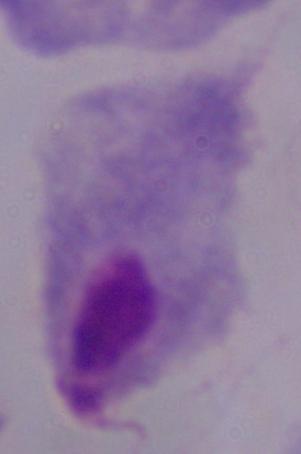
magnification = 1000x
modality = photomicrograph
identification = trichomonad